State which parasite is depicted.
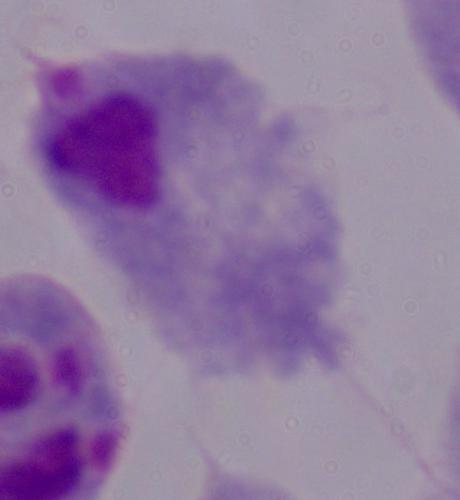

A trichomonad.

Micrograph. Captured at 1000x magnification.